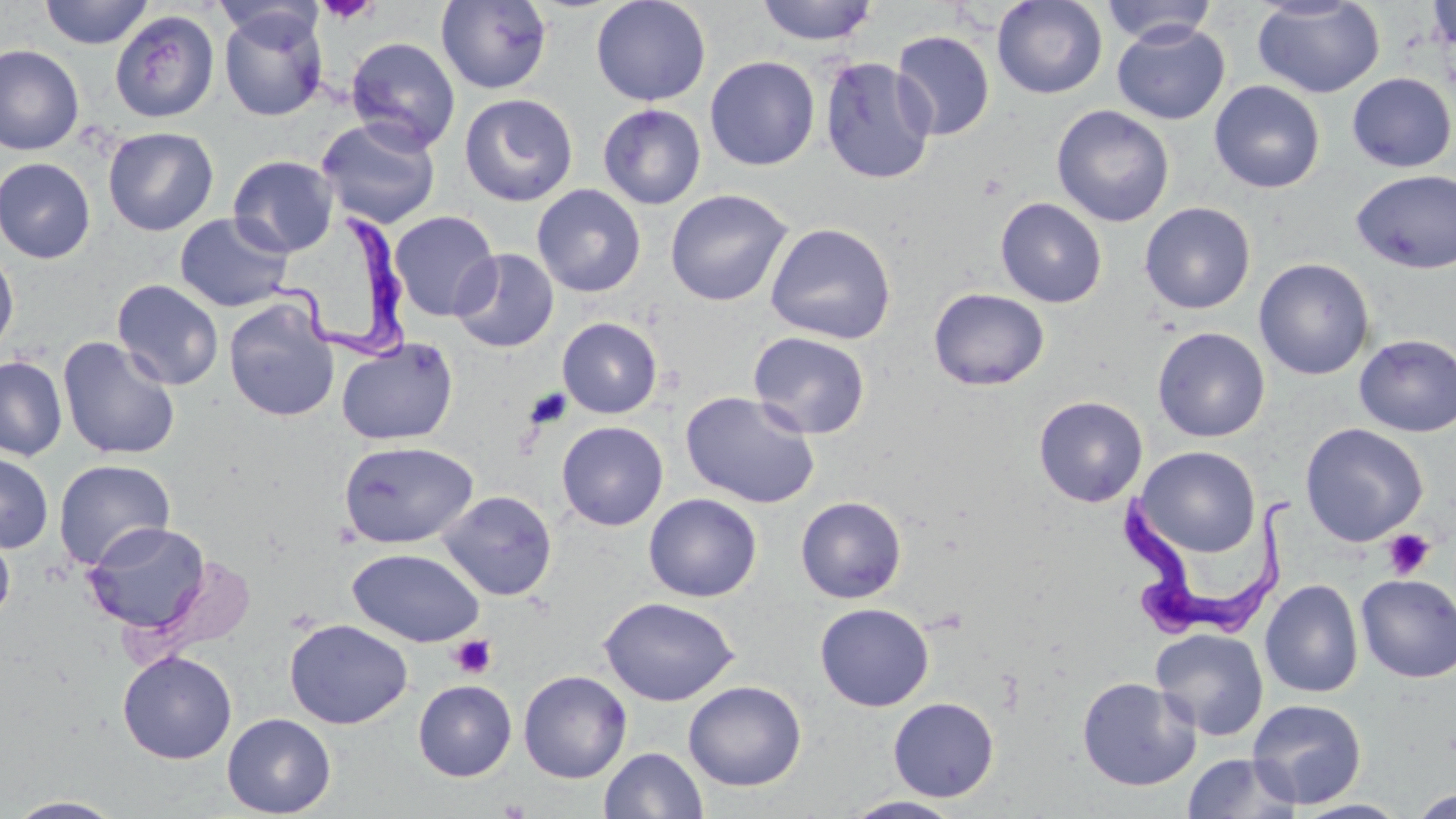
slide_level_diagnosis: Trypanosoma brucei
magnification: 1000x
image_size: 1456×819 pixels
platelet_locations: 'approximate bounding boxes as named x1/y1/x2/y2 corners in pixels: (x1=317, y1=0, x2=379, y2=25), (x1=525, y1=387, x2=572, y2=429), (x1=1383, y1=529, x2=1436, y2=580), (x1=449, y1=635, x2=497, y2=679)'
uninfected_red_blood_cell_locations: 'approximate bounding boxes as named x1/y1/x2/y2 corners in pixels: (x1=39, y1=0, x2=153, y2=49), (x1=436, y1=0, x2=553, y2=94), (x1=590, y1=0, x2=711, y2=106), (x1=755, y1=0, x2=878, y2=46), (x1=992, y1=0, x2=1107, y2=99), (x1=1252, y1=0, x2=1385, y2=98), (x1=1426, y1=0, x2=1456, y2=54), (x1=1101, y1=1, x2=1220, y2=46), (x1=218, y1=7, x2=329, y2=120), (x1=110, y1=10, x2=220, y2=123), (x1=1112, y1=22, x2=1230, y2=125), (x1=892, y1=30, x2=995, y2=141), (x1=345, y1=36, x2=461, y2=153), (x1=0, y1=44, x2=84, y2=156), (x1=704, y1=56, x2=820, y2=171), (x1=820, y1=57, x2=936, y2=185), (x1=1347, y1=72, x2=1455, y2=172), (x1=1209, y1=80, x2=1325, y2=194), (x1=459, y1=93, x2=578, y2=207), (x1=598, y1=103, x2=706, y2=210), (x1=1051, y1=105, x2=1175, y2=227), (x1=316, y1=117, x2=441, y2=229), (x1=102, y1=126, x2=219, y2=235), (x1=228, y1=155, x2=339, y2=257), (x1=0, y1=157, x2=96, y2=263), (x1=1351, y1=169, x2=1456, y2=274), (x1=531, y1=184, x2=646, y2=297), (x1=664, y1=189, x2=793, y2=306), (x1=995, y1=197, x2=1107, y2=308), (x1=1139, y1=202, x2=1256, y2=314), (x1=389, y1=210, x2=501, y2=321), (x1=175, y1=213, x2=293, y2=312), (x1=764, y1=222, x2=897, y2=345), (x1=0, y1=247, x2=19, y2=358), (x1=450, y1=248, x2=559, y2=353), (x1=1254, y1=258, x2=1375, y2=380), (x1=112, y1=279, x2=224, y2=390), (x1=928, y1=287, x2=1050, y2=391), (x1=223, y1=297, x2=340, y2=423), (x1=557, y1=317, x2=663, y2=419), (x1=1152, y1=326, x2=1271, y2=442), (x1=747, y1=331, x2=871, y2=439), (x1=1354, y1=334, x2=1456, y2=437), (x1=57, y1=335, x2=181, y2=461), (x1=336, y1=337, x2=458, y2=445), (x1=0, y1=356, x2=67, y2=460), (x1=680, y1=390, x2=821, y2=509), (x1=1033, y1=395, x2=1148, y2=507), (x1=556, y1=421, x2=668, y2=531), (x1=1300, y1=422, x2=1428, y2=546), (x1=338, y1=440, x2=479, y2=549), (x1=1136, y1=446, x2=1261, y2=557), (x1=0, y1=453, x2=53, y2=552), (x1=53, y1=458, x2=176, y2=570), (x1=439, y1=490, x2=557, y2=601), (x1=643, y1=493, x2=763, y2=602), (x1=796, y1=496, x2=907, y2=603), (x1=82, y1=521, x2=211, y2=635), (x1=0, y1=525, x2=15, y2=627), (x1=347, y1=547, x2=485, y2=647), (x1=1355, y1=574, x2=1456, y2=683), (x1=1260, y1=578, x2=1363, y2=698), (x1=599, y1=596, x2=739, y2=706), (x1=815, y1=602, x2=934, y2=711), (x1=284, y1=618, x2=412, y2=729), (x1=1151, y1=628, x2=1269, y2=740), (x1=118, y1=650, x2=237, y2=764), (x1=518, y1=669, x2=632, y2=783), (x1=1076, y1=676, x2=1200, y2=791), (x1=413, y1=680, x2=517, y2=781), (x1=683, y1=680, x2=807, y2=791), (x1=888, y1=697, x2=999, y2=802), (x1=1247, y1=698, x2=1367, y2=809), (x1=222, y1=713, x2=336, y2=818), (x1=599, y1=747, x2=708, y2=819), (x1=1181, y1=752, x2=1302, y2=819), (x1=1410, y1=788, x2=1456, y2=818), (x1=842, y1=795, x2=966, y2=818), (x1=5, y1=796, x2=127, y2=818), (x1=1294, y1=799, x2=1411, y2=819)'
preparation: thin blood smear
stain: May-Grünwald-Giemsa
field_of_view: one of a larger specimen
modality: optical microscopy
trypanosoma_brucei_locations: 'approximate bounding boxes as named x1/y1/x2/y2 corners in pixels: (x1=289, y1=213, x2=420, y2=359), (x1=1121, y1=487, x2=1303, y2=641)'